Name the blood parasite species.
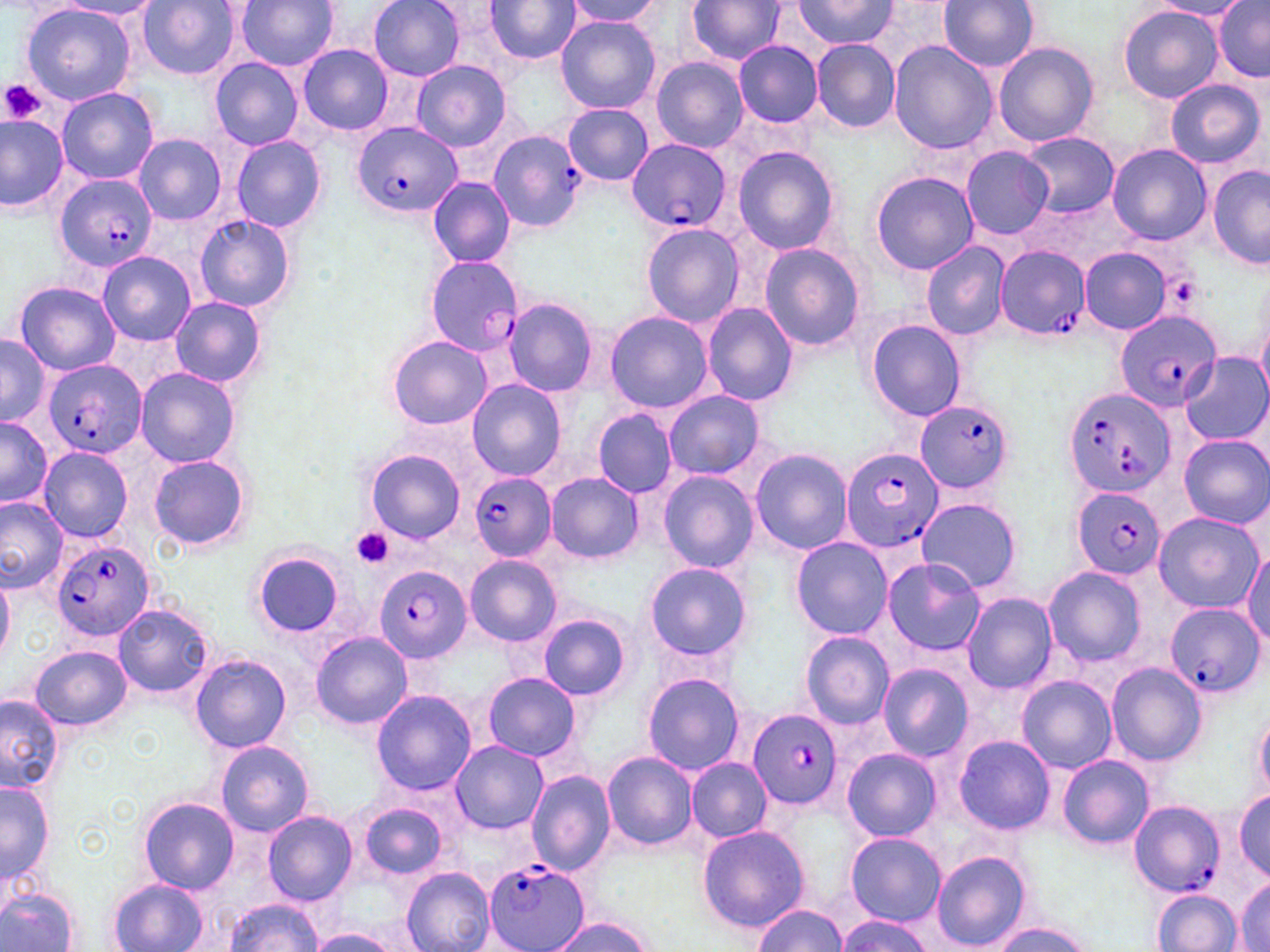

Plasmodium falciparum.

Approximate bounding boxes as named x1/y1/x2/y2 corners in pixels. Platelet locations: (x1=1, y1=79, x2=45, y2=125), (x1=1173, y1=278, x2=1200, y2=304), (x1=351, y1=528, x2=394, y2=568). Plasmodium falciparum-infected red blood cell locations: (x1=353, y1=121, x2=461, y2=216), (x1=487, y1=129, x2=587, y2=234), (x1=626, y1=138, x2=730, y2=233), (x1=55, y1=174, x2=157, y2=272), (x1=994, y1=245, x2=1089, y2=339), (x1=425, y1=256, x2=526, y2=357), (x1=1115, y1=308, x2=1220, y2=412), (x1=41, y1=358, x2=147, y2=460), (x1=1062, y1=386, x2=1176, y2=498), (x1=914, y1=400, x2=1014, y2=494), (x1=841, y1=447, x2=944, y2=553), (x1=469, y1=472, x2=555, y2=561), (x1=1071, y1=485, x2=1166, y2=579), (x1=51, y1=538, x2=157, y2=645), (x1=377, y1=567, x2=471, y2=659), (x1=1166, y1=603, x2=1262, y2=699), (x1=747, y1=709, x2=842, y2=810), (x1=1128, y1=800, x2=1226, y2=899), (x1=484, y1=860, x2=590, y2=952). Uninfected red blood cell locations: (x1=234, y1=0, x2=340, y2=73), (x1=368, y1=0, x2=467, y2=80), (x1=564, y1=0, x2=665, y2=27), (x1=687, y1=0, x2=786, y2=64), (x1=939, y1=0, x2=1039, y2=73), (x1=1213, y1=0, x2=1269, y2=81), (x1=53, y1=1, x2=164, y2=20), (x1=137, y1=1, x2=241, y2=80), (x1=484, y1=1, x2=579, y2=63), (x1=792, y1=1, x2=897, y2=49), (x1=1150, y1=1, x2=1251, y2=19), (x1=19, y1=3, x2=136, y2=106), (x1=1119, y1=5, x2=1222, y2=103), (x1=555, y1=16, x2=661, y2=114), (x1=809, y1=38, x2=901, y2=133), (x1=733, y1=39, x2=823, y2=127), (x1=889, y1=41, x2=996, y2=155), (x1=991, y1=42, x2=1099, y2=147), (x1=297, y1=43, x2=394, y2=135), (x1=651, y1=57, x2=748, y2=152), (x1=209, y1=58, x2=304, y2=150), (x1=411, y1=60, x2=511, y2=150), (x1=1165, y1=79, x2=1265, y2=170), (x1=57, y1=88, x2=159, y2=184), (x1=564, y1=103, x2=653, y2=186), (x1=0, y1=112, x2=70, y2=213), (x1=1021, y1=132, x2=1118, y2=216), (x1=134, y1=134, x2=226, y2=225), (x1=230, y1=134, x2=327, y2=232), (x1=732, y1=146, x2=841, y2=255), (x1=1108, y1=146, x2=1211, y2=245), (x1=960, y1=147, x2=1054, y2=240), (x1=1208, y1=167, x2=1270, y2=267), (x1=870, y1=172, x2=979, y2=275), (x1=428, y1=176, x2=516, y2=266), (x1=195, y1=213, x2=297, y2=313), (x1=640, y1=222, x2=743, y2=329), (x1=921, y1=241, x2=1011, y2=340), (x1=759, y1=243, x2=866, y2=352), (x1=1079, y1=247, x2=1173, y2=334), (x1=98, y1=251, x2=195, y2=344), (x1=14, y1=281, x2=119, y2=375), (x1=169, y1=295, x2=266, y2=388), (x1=501, y1=298, x2=598, y2=395), (x1=702, y1=303, x2=798, y2=406), (x1=604, y1=310, x2=714, y2=414), (x1=867, y1=319, x2=965, y2=422), (x1=0, y1=333, x2=48, y2=425), (x1=386, y1=334, x2=491, y2=430), (x1=1179, y1=353, x2=1269, y2=446), (x1=135, y1=367, x2=241, y2=469), (x1=466, y1=379, x2=565, y2=483), (x1=663, y1=389, x2=764, y2=478), (x1=593, y1=409, x2=676, y2=498), (x1=0, y1=416, x2=51, y2=508), (x1=1180, y1=435, x2=1270, y2=529), (x1=38, y1=446, x2=133, y2=543), (x1=366, y1=449, x2=466, y2=545), (x1=750, y1=449, x2=852, y2=554), (x1=149, y1=453, x2=253, y2=552), (x1=659, y1=471, x2=759, y2=572), (x1=547, y1=473, x2=642, y2=562), (x1=0, y1=496, x2=68, y2=593), (x1=917, y1=496, x2=1022, y2=595), (x1=1151, y1=512, x2=1263, y2=613), (x1=790, y1=537, x2=893, y2=640), (x1=1243, y1=545, x2=1270, y2=649), (x1=252, y1=552, x2=348, y2=637), (x1=465, y1=555, x2=561, y2=647), (x1=880, y1=557, x2=986, y2=657), (x1=644, y1=562, x2=751, y2=660), (x1=1044, y1=565, x2=1146, y2=667), (x1=962, y1=592, x2=1057, y2=693), (x1=113, y1=603, x2=214, y2=697), (x1=538, y1=614, x2=631, y2=700), (x1=800, y1=631, x2=894, y2=729), (x1=309, y1=632, x2=413, y2=731), (x1=30, y1=645, x2=131, y2=731), (x1=190, y1=653, x2=292, y2=753), (x1=1105, y1=662, x2=1208, y2=766), (x1=878, y1=663, x2=973, y2=760), (x1=482, y1=672, x2=582, y2=762), (x1=642, y1=672, x2=745, y2=774), (x1=1018, y1=676, x2=1116, y2=772), (x1=372, y1=690, x2=476, y2=796), (x1=1, y1=694, x2=63, y2=792), (x1=1254, y1=703, x2=1270, y2=799), (x1=952, y1=734, x2=1054, y2=835), (x1=215, y1=741, x2=313, y2=836), (x1=451, y1=741, x2=545, y2=832), (x1=842, y1=747, x2=942, y2=843), (x1=600, y1=752, x2=698, y2=850), (x1=1057, y1=754, x2=1154, y2=850), (x1=686, y1=757, x2=771, y2=841), (x1=527, y1=769, x2=616, y2=877), (x1=0, y1=780, x2=53, y2=886), (x1=1233, y1=791, x2=1270, y2=880), (x1=140, y1=797, x2=237, y2=894), (x1=357, y1=801, x2=448, y2=880), (x1=262, y1=810, x2=357, y2=906), (x1=698, y1=825, x2=809, y2=930), (x1=845, y1=832, x2=945, y2=925), (x1=930, y1=850, x2=1032, y2=950), (x1=402, y1=868, x2=495, y2=952), (x1=1236, y1=875, x2=1269, y2=952), (x1=107, y1=878, x2=207, y2=952), (x1=1, y1=887, x2=80, y2=952), (x1=1153, y1=889, x2=1241, y2=951), (x1=221, y1=899, x2=324, y2=951), (x1=751, y1=903, x2=848, y2=951), (x1=837, y1=915, x2=935, y2=952), (x1=551, y1=917, x2=652, y2=952), (x1=991, y1=922, x2=1092, y2=952), (x1=308, y1=928, x2=401, y2=952). May-Grünwald-Giemsa-stained preparation. Thin blood smear. Image is 1270×952 pixels. 1000x magnification. Single field of view. Optical microscopy.